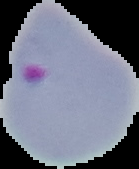
Cell region segmented out of the field of view; the surrounding area is masked to black. Image is 139×169 pixels. Result: malaria parasites identified. From a thin blood smear.